Report the malaria status of this cell.
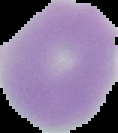
It is uninfected.

{
  "image_type": "segmented cell region with the area outside set to black",
  "image_size": "118×133 pixels",
  "preparation": "thin blood smear"
}